Assess this cell for malaria.
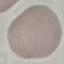

Uninfected.

image type = automatically extracted cell patch, resized to 64 × 64 pixels
preparation = thin blood smear
stain = Giemsa
capture = smartphone camera at the microscope eyepiece